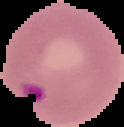 Result: malaria parasites identified. The area outside the segmented cell region is set to black. Image is 124×127 pixels. From a thin blood film.